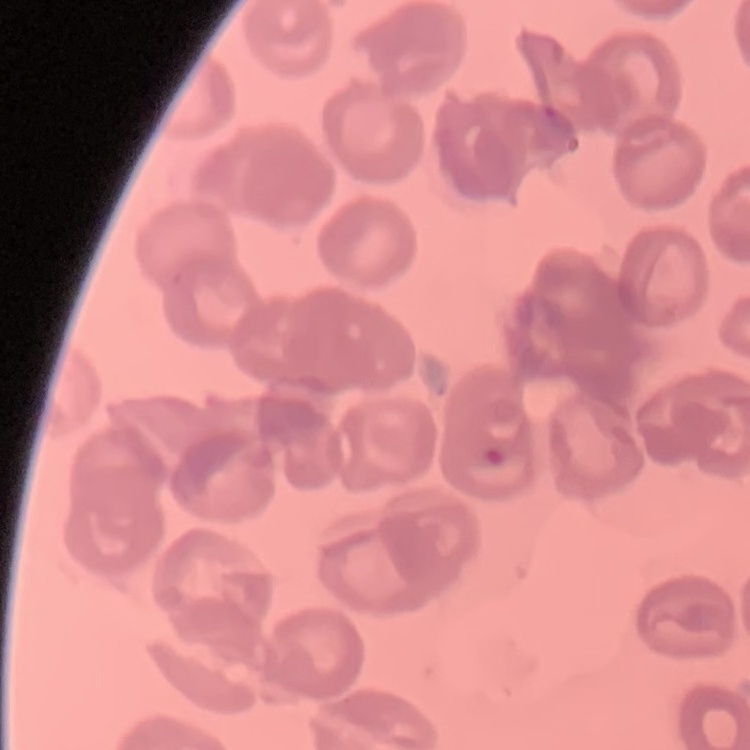

{
  "red_blood_cell_morphology": "no rouleaux formation",
  "preparation": "thin blood smear",
  "image_type": "square crop of a larger photomicrograph",
  "stain": "Field's or Giemsa"
}